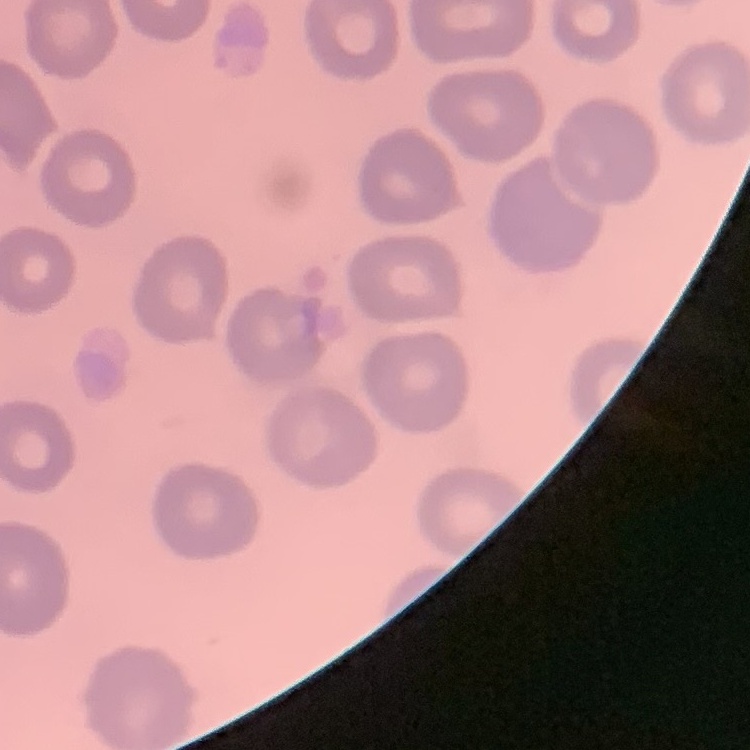

{
  "erythrocyte_morphology": "no rouleaux formation",
  "image_type": "one tile cut from a larger photomicrograph",
  "stain": "Field's or Giemsa",
  "preparation": "thin blood film"
}